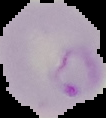
Summary:
  - Image type: segmented cell region with the area outside set to black
  - Malaria status: parasitized
  - Image size: 106×118 pixels
  - Preparation: thin blood smear